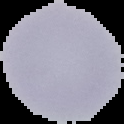

malaria status = uninfected
preparation = thin blood film
image type = segmented cell region on a black background
image size = 124×124 pixels